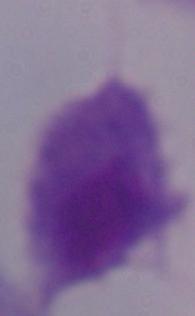
modality = photomicrograph
magnification = 1000x
identification = trichomonad